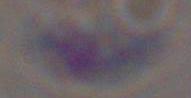
Summary:
  - Modality: micrograph
  - Magnification: 1000x
  - Identification: Toxoplasma gondii